Name the cell type shown.
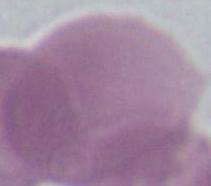

An erythrocyte.

modality = micrograph
magnification = 1000x